Identify the cell.
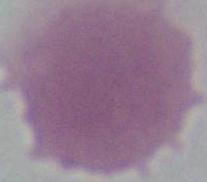

An erythrocyte.

{
  "magnification": "1000x",
  "modality": "micrograph"
}